Assess the morphology of the erythrocytes.
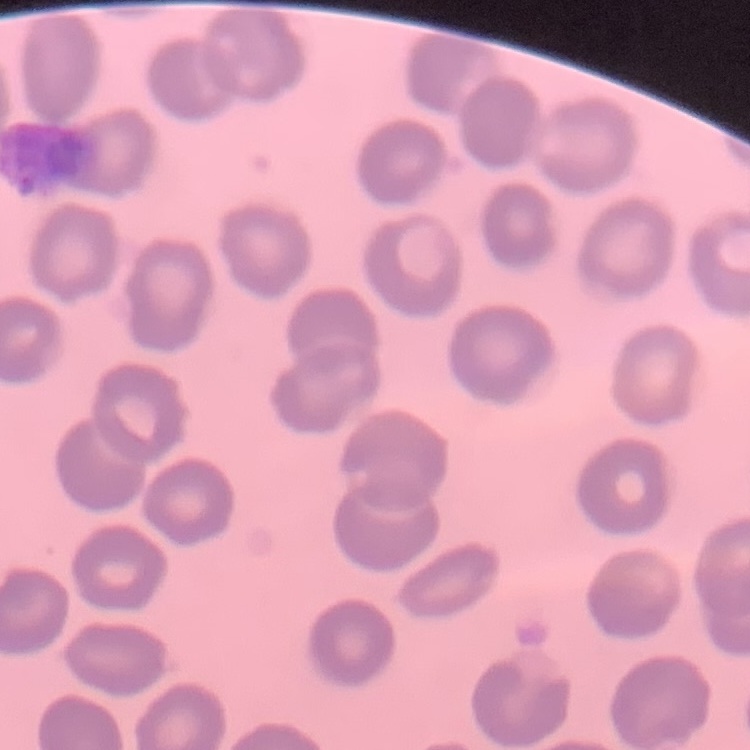

No rouleaux formation.

{
  "preparation": "thin blood film",
  "stain": "Field's or Giemsa",
  "image_type": "one tile cut from a larger photomicrograph"
}